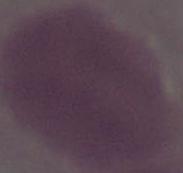
{
  "identification": "erythrocyte",
  "modality": "photomicrograph",
  "magnification": "1000x"
}